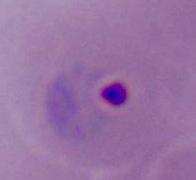

Summary:
  - Magnification: 400x or 1000x
  - Modality: photomicrograph
  - Identification: Plasmodium